Point out Plasmodium parasites and leukocytes.
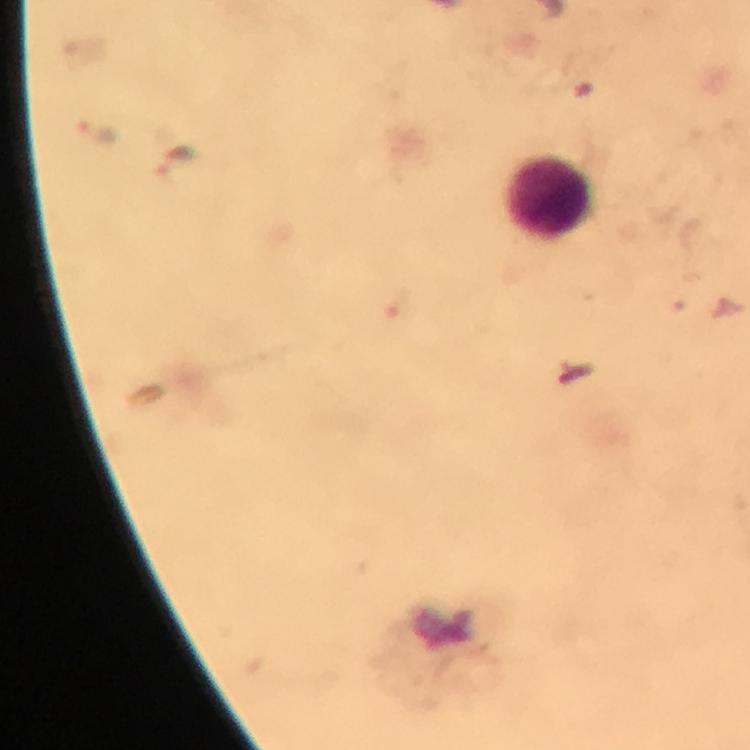

Approximate centers as {x, y} in pixels.
Plasmodium parasites: {96, 131}, {172, 162}, {396, 304}.
Leukocytes: {550, 196}.

From a diagnostic examination for malaria. Image is 750×750 pixels. Cropped region of a single field of view. Immersion oil was used. Smartphone photograph taken through a microscope. Giemsa-stained preparation. Thick blood smear. 100x magnification.